Name the cell type shown.
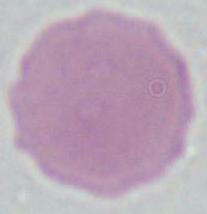

This is an erythrocyte.

Summary:
  - Magnification: 1000x
  - Modality: photomicrograph